Comment on the morphology of the red blood cells.
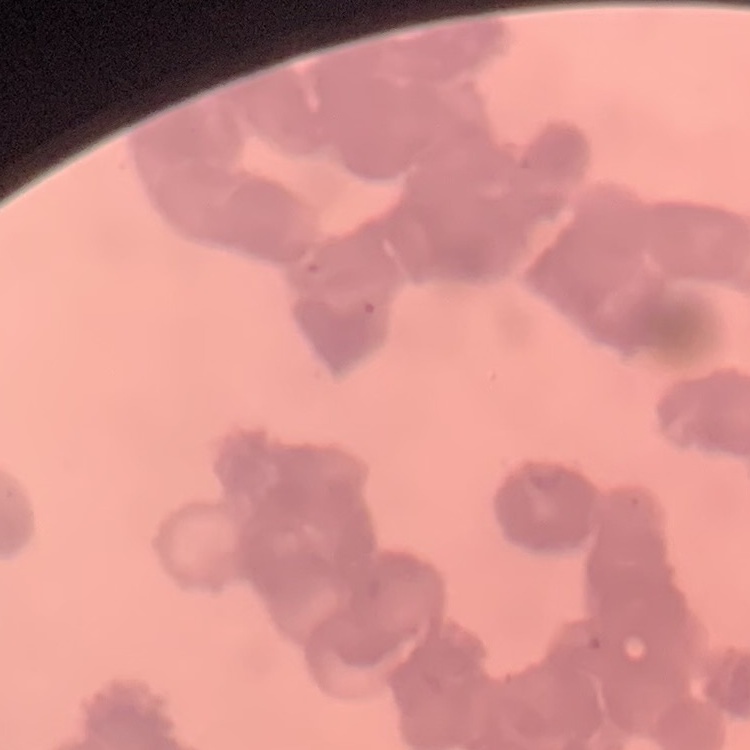

They show rouleaux formation.

Stained with either Field's or Giemsa. Thin peripheral smear. One tile cut from a larger photomicrograph.